Identify the blood parasite species.
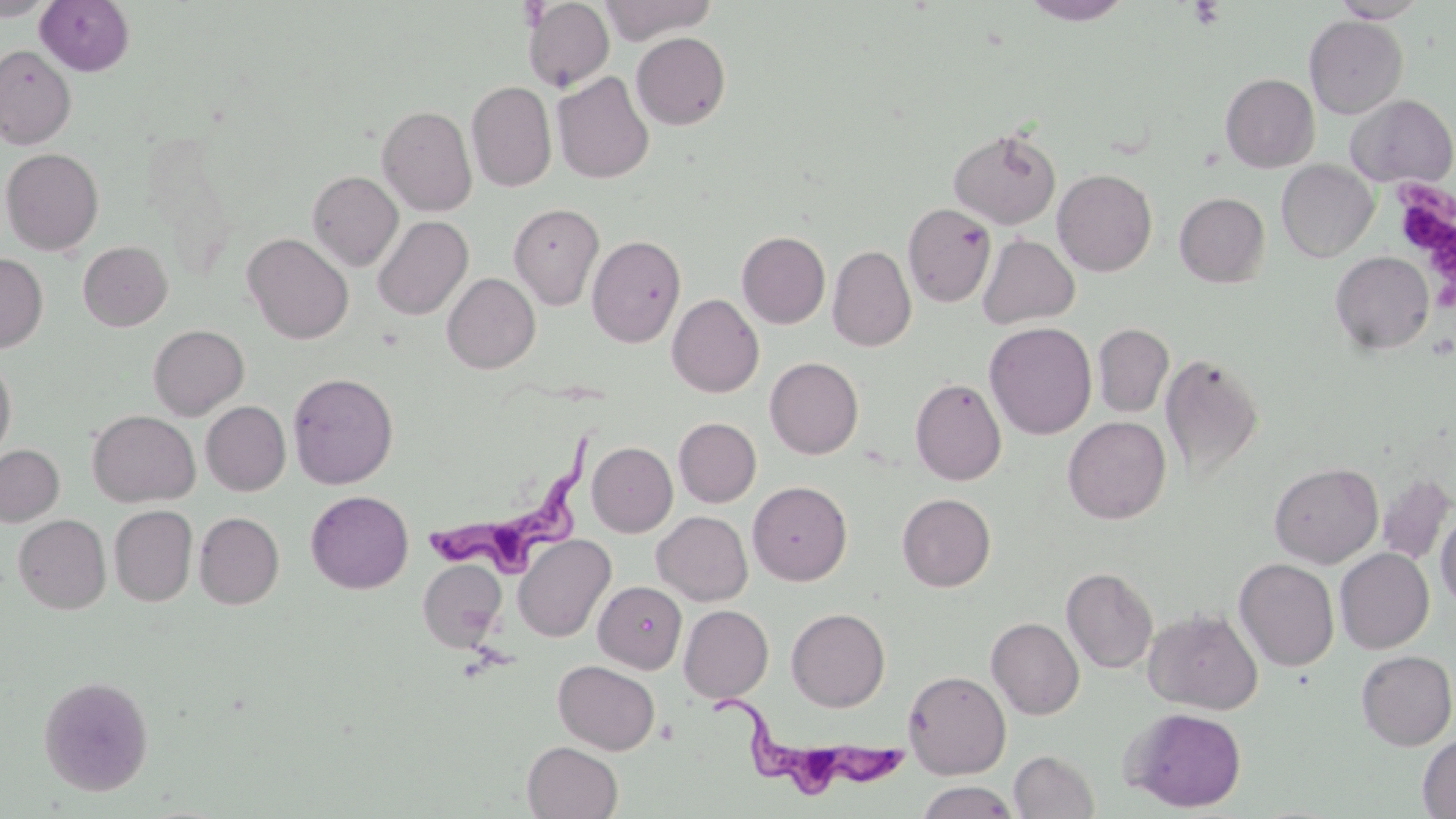
Trypanosoma brucei.

uninfected_red_blood_cell_locations: 'approximate bounding boxes as (x1, y1, x2, y2) in pixels: (0, 0, 55, 20), (522, 0, 614, 92), (599, 0, 718, 44), (1020, 0, 1134, 25), (1331, 0, 1429, 22), (35, 1, 134, 75), (1304, 15, 1408, 119), (631, 32, 731, 130), (0, 45, 76, 148), (552, 71, 654, 184), (1220, 73, 1319, 172), (467, 81, 557, 192), (1345, 94, 1455, 187), (376, 104, 477, 216), (143, 126, 241, 280), (948, 126, 1061, 229), (1, 148, 104, 255), (1276, 160, 1379, 262), (1053, 168, 1157, 276), (307, 170, 403, 271), (1175, 192, 1270, 287), (509, 203, 605, 311), (903, 203, 996, 307), (373, 215, 473, 320), (737, 231, 830, 328), (242, 233, 354, 344), (977, 233, 1079, 329), (587, 235, 686, 347), (78, 241, 172, 331), (827, 245, 916, 352), (1330, 251, 1435, 355), (0, 253, 48, 353), (442, 273, 540, 373), (667, 293, 764, 398), (984, 322, 1097, 439), (1093, 323, 1174, 417), (148, 324, 249, 419), (1160, 352, 1265, 481), (0, 354, 17, 463), (765, 356, 864, 459), (287, 372, 398, 489), (910, 378, 1006, 485), (201, 401, 291, 496), (87, 410, 200, 507), (1063, 416, 1171, 524), (674, 417, 761, 507), (587, 442, 677, 537), (0, 444, 64, 526), (1268, 462, 1384, 568), (1376, 472, 1454, 566), (748, 480, 853, 585), (306, 490, 413, 593), (897, 493, 996, 592), (109, 505, 197, 606), (1436, 508, 1456, 610), (194, 511, 285, 609), (652, 511, 752, 606), (13, 514, 111, 614), (513, 534, 617, 643), (1335, 548, 1434, 653), (418, 558, 506, 651), (1234, 558, 1339, 671), (1062, 567, 1158, 674), (594, 581, 687, 673), (679, 604, 773, 703), (1143, 607, 1264, 714), (786, 608, 890, 711), (986, 617, 1084, 719), (1356, 650, 1456, 750), (552, 660, 660, 755), (904, 669, 1011, 779), (37, 675, 154, 796), (1123, 707, 1247, 812), (1418, 733, 1456, 818), (522, 741, 622, 819), (1009, 749, 1100, 818), (915, 781, 1020, 819)'
platelet_locations: 'approximate bounding boxes as (x1, y1, x2, y2) in pixels: (1189, 1, 1226, 28), (1391, 177, 1456, 310)'
stain: May-Grünwald-Giemsa
modality: optical microscopy
preparation: thin blood smear
image_size: 1456×819 pixels
magnification: 1000x
trypanosoma_brucei_locations: 'approximate bounding boxes as (x1, y1, x2, y2) in pixels: (433, 428, 606, 570), (698, 694, 904, 796)'
field_of_view: single